Outline each blood parasite and name the species.
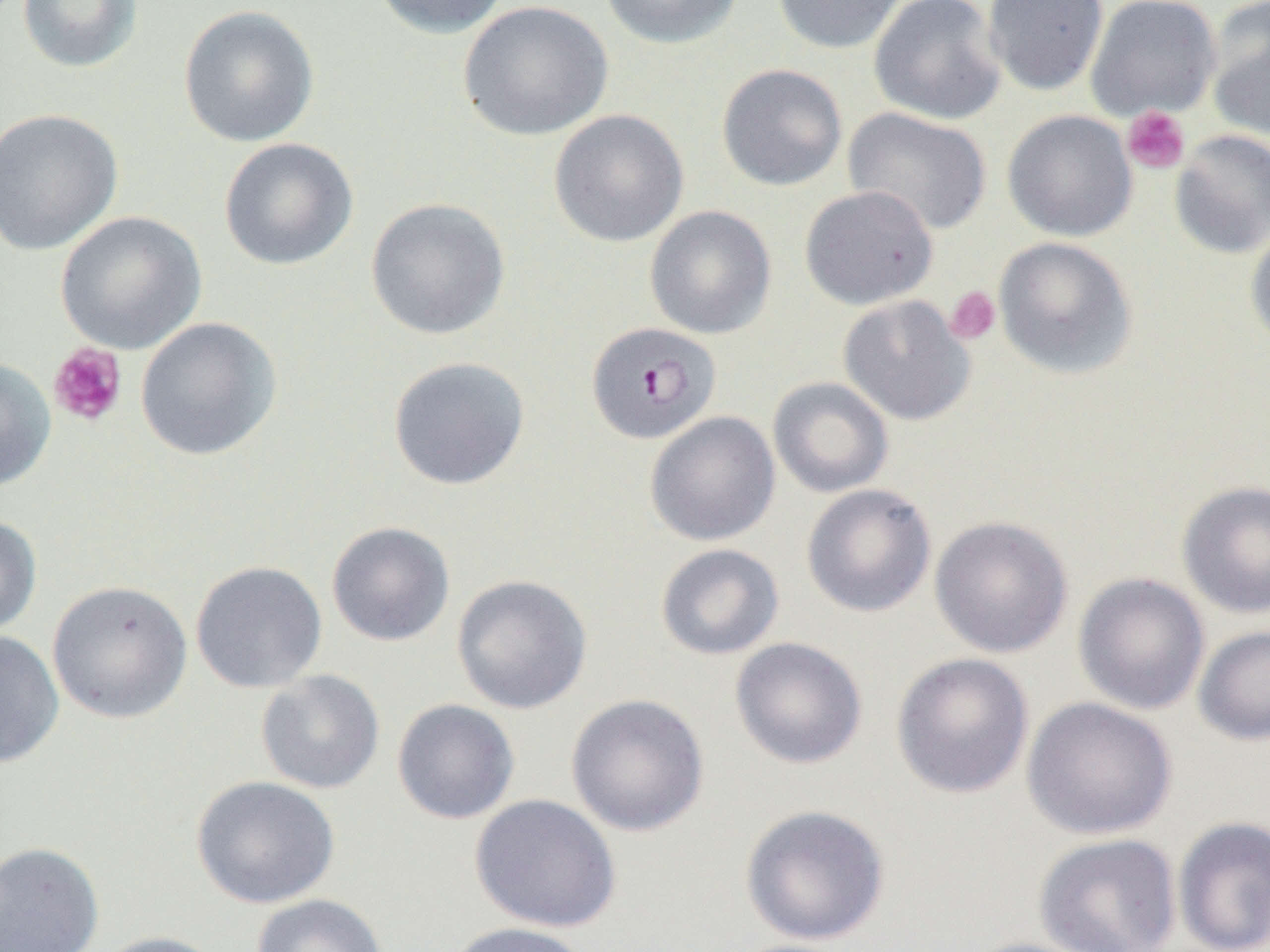
Approximate bounding boxes as [x1, y1, x2, y2] in pixels.
Plasmodium falciparum-infected red blood cells: [585, 321, 722, 445].
No Plasmodium ovale, Plasmodium malariae, Plasmodium vivax, Babesia divergens, or Trypanosoma brucei observed.

slide-level diagnosis = Plasmodium falciparum
image size = 1270×952 pixels
modality = light microscopy
uninfected red blood cell locations = approximate bounding boxes as [x1, y1, x2, y2] in pixels: [16, 0, 144, 74], [371, 0, 511, 39], [598, 0, 744, 49], [771, 0, 910, 54], [868, 0, 1007, 125], [982, 0, 1109, 96], [1085, 0, 1222, 121], [458, 1, 613, 141], [1205, 2, 1270, 142], [178, 5, 320, 147], [716, 63, 848, 191], [0, 107, 124, 256], [842, 107, 992, 236], [548, 109, 690, 247], [1002, 109, 1138, 242], [1169, 129, 1270, 260], [218, 137, 359, 270], [799, 185, 939, 311], [365, 197, 511, 341], [644, 205, 776, 339], [56, 210, 207, 354], [1245, 221, 1270, 351], [992, 236, 1138, 380], [838, 294, 976, 426], [135, 316, 282, 461], [387, 356, 531, 491], [0, 357, 56, 492], [767, 376, 894, 499], [644, 411, 781, 547], [1176, 479, 1270, 618], [801, 483, 937, 617], [0, 514, 42, 639], [929, 515, 1073, 658], [326, 521, 455, 647], [655, 543, 785, 661], [190, 560, 327, 693], [1072, 572, 1210, 715], [451, 574, 593, 714], [47, 580, 193, 724], [1193, 624, 1270, 746], [0, 629, 65, 769], [729, 636, 868, 769], [890, 652, 1035, 799], [255, 669, 385, 794], [566, 693, 711, 837], [1022, 696, 1177, 840], [391, 698, 520, 825], [191, 775, 341, 909], [469, 794, 621, 933], [739, 804, 891, 946], [1172, 816, 1270, 952], [1034, 833, 1181, 952], [0, 841, 104, 951], [251, 893, 388, 952], [443, 921, 593, 952], [91, 931, 227, 952], [959, 937, 1100, 952]
field of view = one of a larger specimen
preparation = thin blood film
magnification = 1000x
platelet locations = approximate bounding boxes as [x1, y1, x2, y2] in pixels: [1121, 106, 1190, 174], [945, 286, 1001, 345], [48, 343, 127, 427]